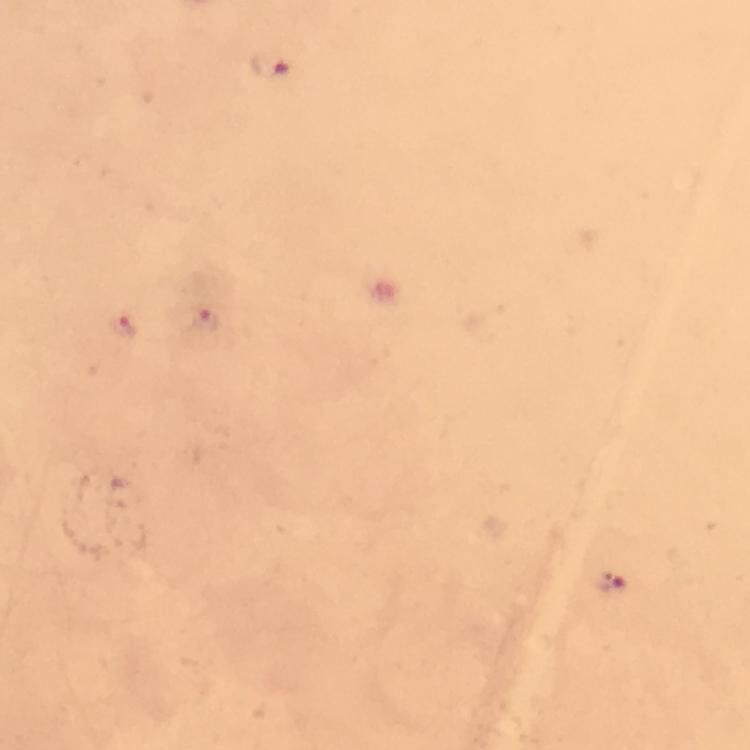
Approximate centers as (x, y) in pixels. Malaria parasite locations: (271, 65), (206, 320), (124, 329), (607, 579). Thick blood smear. From a malaria diagnostic workup. Cropped region of a single field of view. Giemsa stain. Image is 750×750 pixels. Photographed through the microscope with a smartphone camera. Immersion oil applied. 100x magnification.